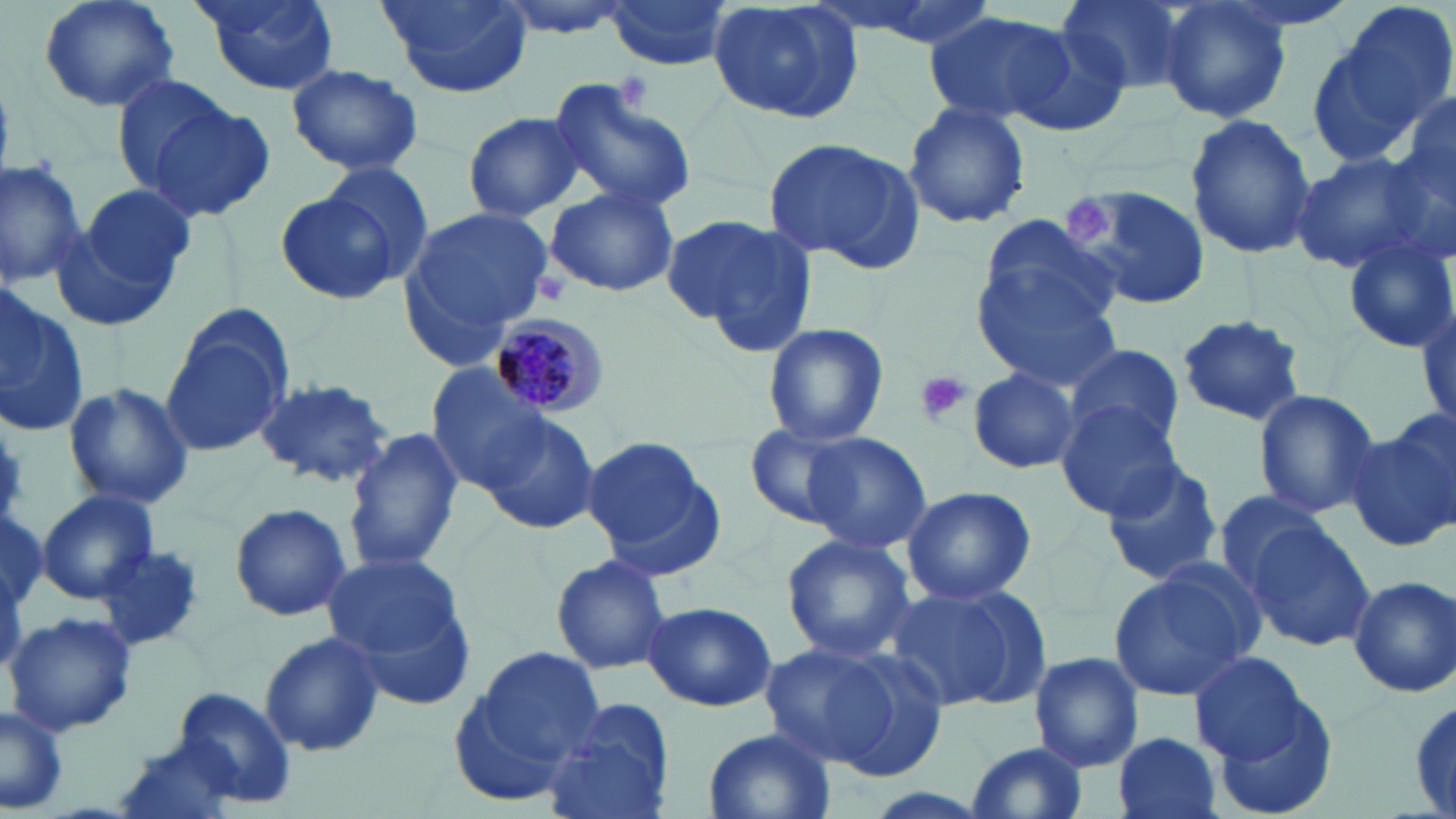

Approximate bounding boxes as (x1, y1, x2, y2) in pixels. Plasmodium malariae-infected red blood cell locations: (489, 309, 611, 420). Platelet locations: (618, 74, 653, 110), (1068, 195, 1117, 245), (531, 272, 571, 306), (915, 369, 973, 428). Uninfected red blood cell locations: (36, 0, 181, 112), (190, 0, 342, 96), (380, 0, 532, 97), (491, 0, 634, 36), (601, 0, 736, 70), (806, 0, 1003, 47), (1053, 0, 1191, 95), (1315, 0, 1456, 165), (705, 1, 868, 124), (1157, 3, 1293, 124), (925, 11, 1080, 128), (1004, 24, 1138, 139), (286, 63, 424, 177), (109, 69, 240, 191), (547, 78, 697, 215), (1397, 94, 1455, 204), (144, 100, 275, 223), (902, 101, 1031, 230), (462, 111, 590, 222), (1184, 115, 1317, 258), (763, 135, 924, 272), (1289, 151, 1439, 276), (0, 156, 88, 286), (321, 160, 434, 281), (1058, 184, 1209, 315), (66, 185, 194, 318), (545, 186, 678, 299), (276, 188, 402, 303), (401, 205, 553, 358), (974, 210, 1126, 344), (664, 214, 817, 353), (1340, 232, 1455, 355), (975, 263, 1124, 389), (0, 295, 92, 438), (158, 309, 294, 460), (1173, 313, 1307, 428), (761, 322, 889, 448), (1063, 341, 1185, 452), (425, 367, 555, 494), (968, 367, 1081, 475), (253, 375, 398, 489), (65, 382, 193, 510), (1252, 389, 1382, 517), (1057, 400, 1186, 520), (480, 414, 601, 537), (1349, 418, 1456, 552), (743, 422, 864, 531), (344, 426, 465, 574), (798, 432, 932, 553), (584, 437, 715, 561), (1101, 458, 1225, 587), (902, 485, 1037, 606), (1209, 489, 1334, 600), (37, 490, 157, 604), (228, 502, 353, 622), (0, 512, 47, 614), (1241, 520, 1375, 651), (781, 535, 915, 661), (97, 544, 209, 652), (322, 554, 466, 659), (550, 554, 671, 674), (1105, 562, 1260, 704), (1349, 575, 1456, 698), (886, 581, 1049, 715), (644, 601, 776, 713), (3, 610, 139, 735), (259, 632, 386, 757), (763, 638, 943, 779), (460, 646, 608, 791), (1189, 651, 1312, 763), (1027, 652, 1143, 771), (1207, 685, 1341, 817), (174, 686, 299, 809), (1407, 689, 1456, 819), (544, 697, 675, 819), (0, 707, 68, 814), (701, 727, 835, 819), (1112, 732, 1224, 819), (117, 739, 237, 819), (964, 739, 1089, 819). Slide-level diagnosis: Plasmodium malariae. Image is 1456×819 pixels. Light microscopy. 1000x magnification. Thin blood smear. One field of a larger specimen. May-Grünwald-Giemsa stain.